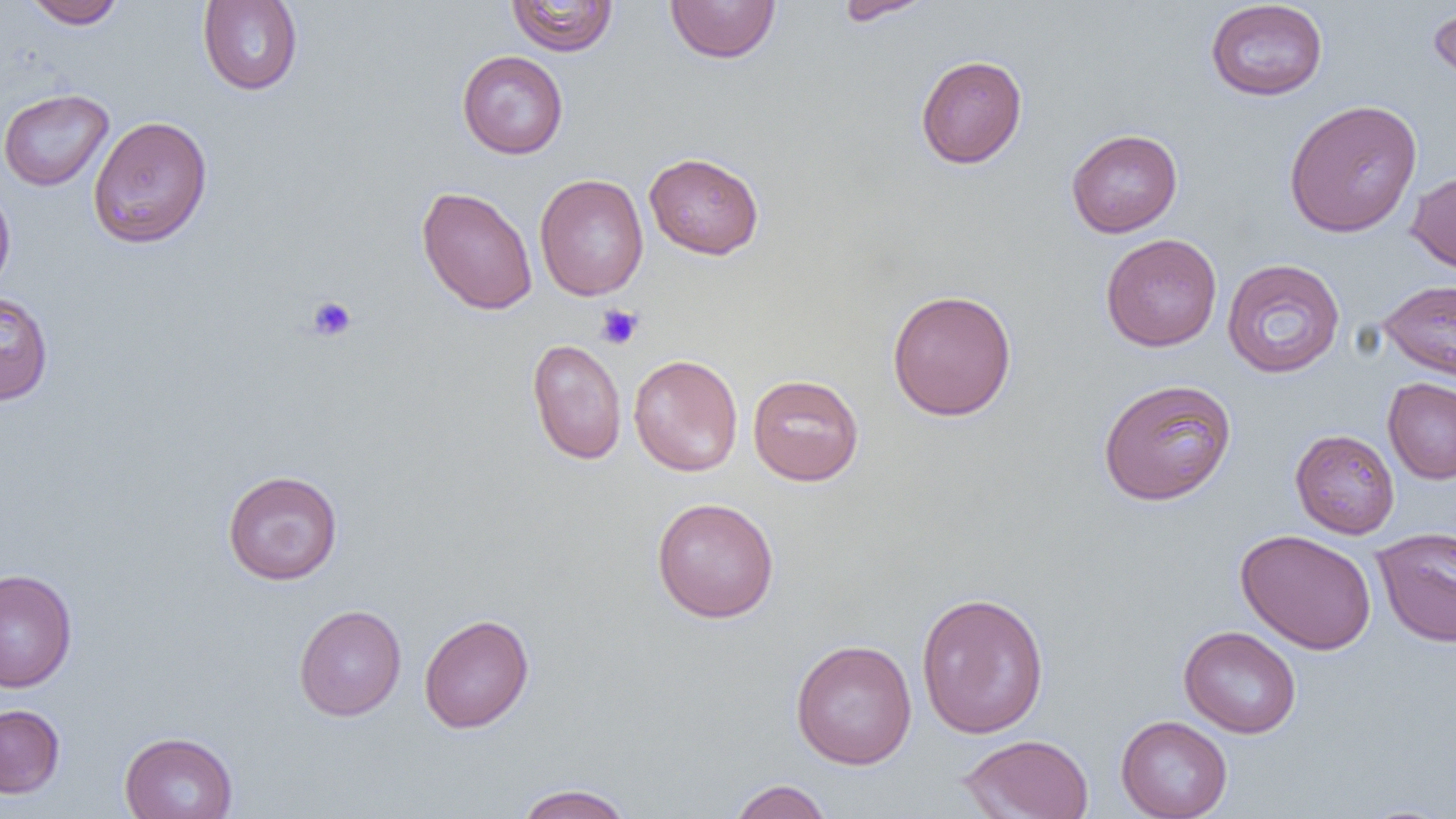
slide_level_diagnosis: negative for blood parasites
magnification: 1000x
preparation: thin blood smear
uninfected_red_blood_cell_locations: 'approximate bounding boxes as (x1,y1)-(x2,y2) corner pairs in pixels: (23,0)-(126,29), (197,0)-(303,95), (506,0)-(619,56), (665,0)-(781,64), (834,0)-(936,25), (1204,0)-(1329,101), (1428,3)-(1456,89), (457,50)-(569,159), (915,54)-(1028,168), (0,88)-(114,191), (1283,99)-(1422,238), (88,115)-(213,249), (1066,129)-(1183,237), (644,151)-(765,259), (1406,169)-(1456,276), (534,174)-(648,301), (0,179)-(16,298), (416,186)-(537,315), (1100,233)-(1222,352), (1221,259)-(1345,378), (1378,278)-(1456,382), (886,289)-(1017,421), (0,291)-(54,405), (527,338)-(627,465), (628,354)-(743,477), (747,373)-(864,486), (1383,377)-(1456,484), (1098,378)-(1237,506), (1290,429)-(1400,539), (222,469)-(343,585), (651,497)-(780,622), (1372,526)-(1456,648), (1235,528)-(1377,655), (0,568)-(77,693), (915,590)-(1050,739), (293,604)-(406,721), (418,613)-(534,733), (1178,625)-(1302,738), (791,639)-(917,769), (0,704)-(65,799), (1115,715)-(1233,819), (119,730)-(238,819), (958,733)-(1095,819), (727,779)-(835,819), (513,783)-(635,819)'
image_size: 1456×819 pixels
field_of_view: one of a larger specimen
modality: light microscopy
platelet_locations: 'approximate bounding boxes as (x1,y1)-(x2,y2) corner pairs in pixels: (306,295)-(357,342), (594,304)-(644,350)'